Point out Plasmodium parasites and leukocytes.
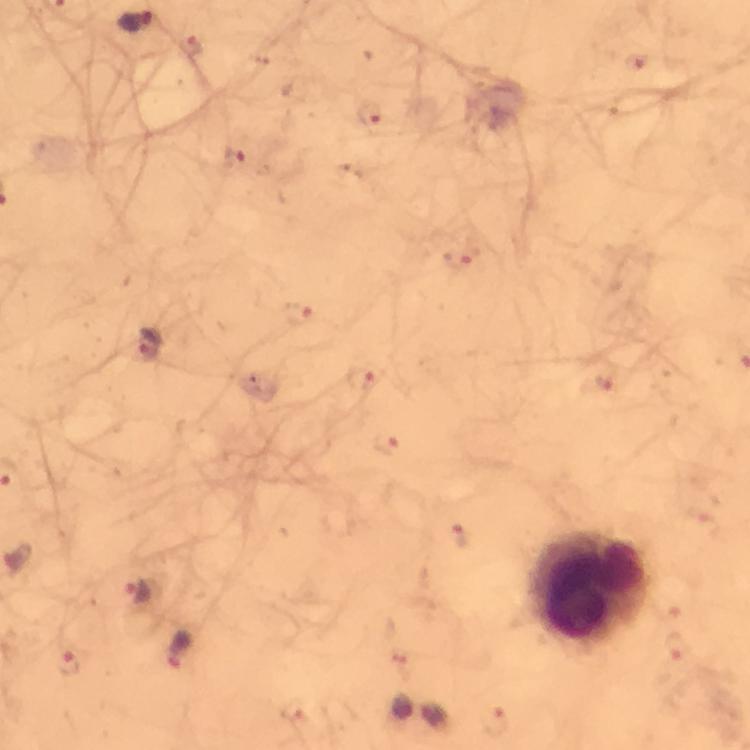
Approximate object centers, in pixels from the top-left corner.
Plasmodium parasites: (x=195, y=47), (x=637, y=65), (x=374, y=118), (x=237, y=161), (x=460, y=260), (x=299, y=316), (x=150, y=343), (x=364, y=379), (x=606, y=383), (x=388, y=446), (x=462, y=534), (x=140, y=595), (x=673, y=613), (x=681, y=650), (x=180, y=651), (x=71, y=664), (x=296, y=711), (x=499, y=721).
Leukocytes: (x=591, y=589).

Summary:
  - Context: from a malaria diagnostic workup
  - Stain: Giemsa
  - Cropped from: a single field of view
  - Preparation: thick blood smear
  - Immersion oil: applied
  - Magnification: 100x
  - Capture: smartphone mounted on the microscope
  - Image size: 750×750 pixels